Name the parasite shown.
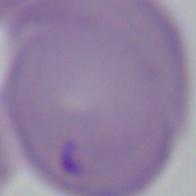
Babesia.

Photomicrograph. Captured at 1000x magnification.